Assess the morphology of the erythrocytes.
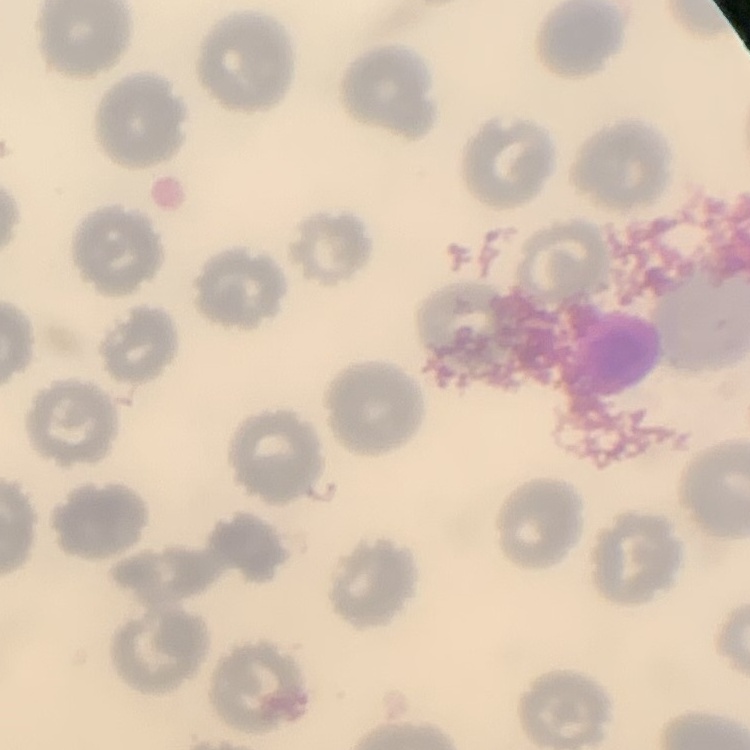
No rouleaux formation.

stain = Field's or Giemsa
preparation = thin peripheral smear
image type = one tile cut from a larger photomicrograph